Classify this cell by malaria status.
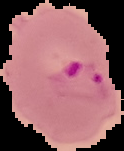

Parasitized.

{
  "preparation": "thin blood smear",
  "image_type": "segmented cell region with the area outside set to black",
  "image_size": "124×151 pixels"
}